Give the position of every Plasmodium parasite.
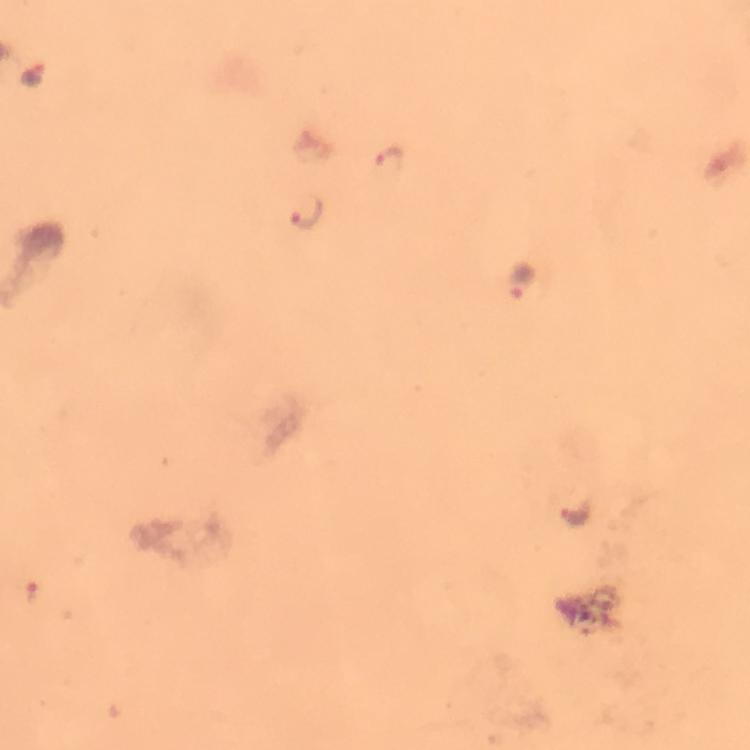
Approximate centers as [x, y] in pixels.
Plasmodium parasites: [386, 161], [304, 213], [521, 282], [573, 513], [32, 592].

context = from a diagnostic examination for malaria
preparation = thick smear
capture = smartphone camera through the microscope
cropped from = a single field of view
image size = 750×750 pixels
stain = Giemsa
magnification = 100x
immersion oil = used